Classify this cell by malaria status.
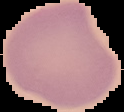

Uninfected.

From a thin blood smear. Image is 124×112 pixels. Cell region segmented out of the field of view; the surrounding area is masked to black.